Classify this cell by malaria status.
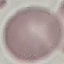
It is uninfected.

{
  "image_type": "automatically extracted cell patch, resized to 64 × 64 pixels",
  "preparation": "thin smear",
  "capture": "smartphone camera at the microscope eyepiece",
  "stain": "Giemsa"
}